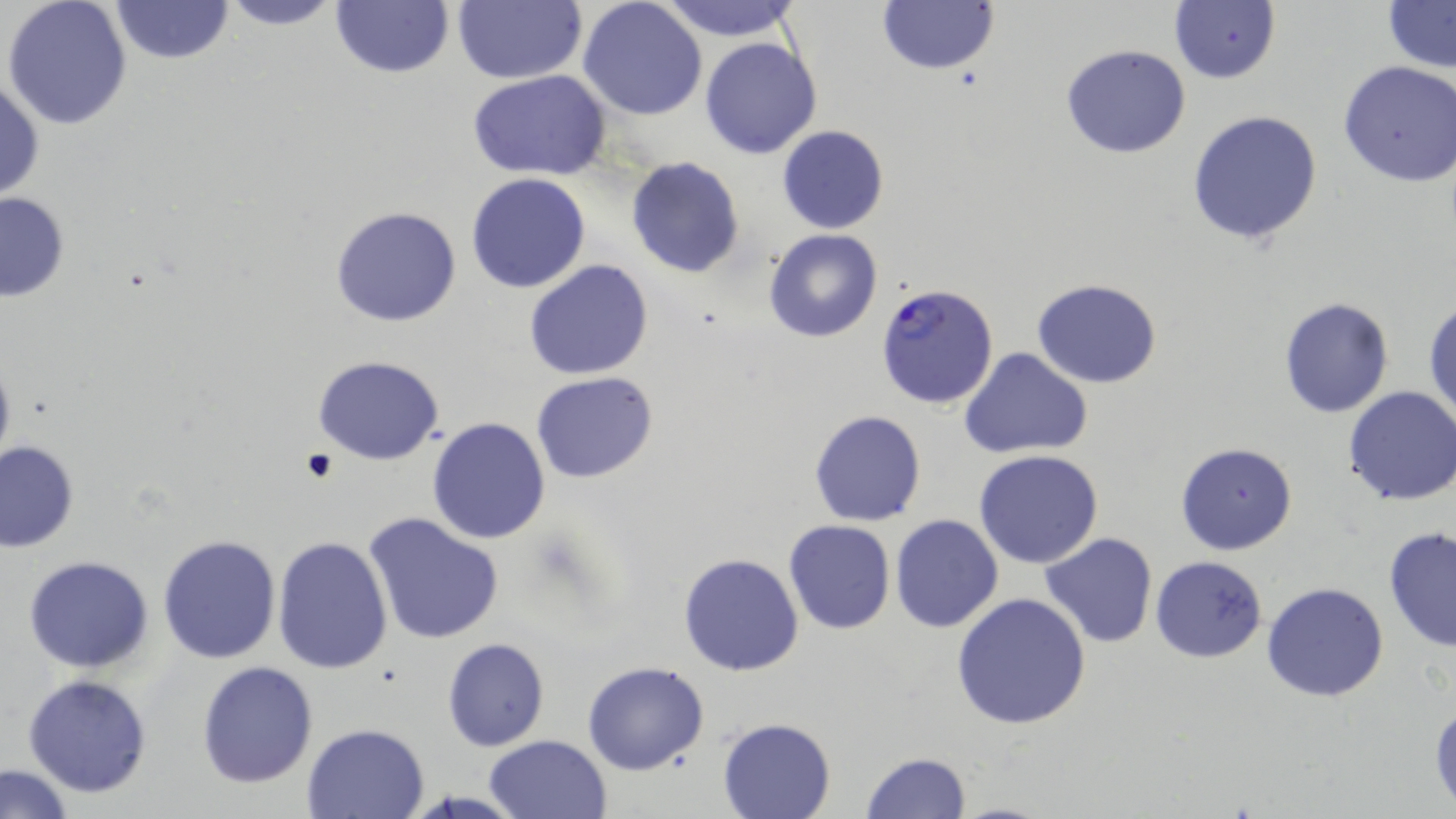
slide-level diagnosis = Plasmodium falciparum
stain = May-Grünwald-Giemsa
image size = 1456×819 pixels
preparation = thin blood film
magnification = 1000x
Plasmodium falciparum-infected red blood cell locations = approximate bounding boxes as (x1,y1)-(x2,y2) corner pairs in pixels: (876,282)-(1002,411)
field of view = one of a larger specimen
uninfected red blood cell locations = approximate bounding boxes as (x1,y1)-(x2,y2) corner pairs in pixels: (2,0)-(132,130), (216,0)-(347,30), (331,0)-(453,79), (453,0)-(586,85), (657,0)-(804,41), (110,1)-(235,65), (577,1)-(707,120), (878,1)-(1000,74), (1381,1)-(1456,72), (1169,2)-(1280,85), (700,36)-(822,158), (1060,44)-(1191,160), (1338,60)-(1456,187), (469,69)-(612,180), (0,75)-(44,203), (1187,110)-(1324,247), (776,125)-(890,234), (625,157)-(744,279), (466,172)-(593,293), (0,191)-(71,305), (331,205)-(463,328), (763,228)-(884,343), (524,259)-(654,381), (1032,278)-(1163,387), (1278,297)-(1395,418), (1425,298)-(1456,426), (960,345)-(1094,459), (0,352)-(16,475), (313,355)-(443,463), (531,372)-(659,484), (1342,386)-(1456,505), (808,409)-(927,527), (427,418)-(550,543), (1,441)-(78,553), (1175,441)-(1298,556), (975,450)-(1104,568), (364,512)-(506,646), (890,513)-(1004,633), (784,520)-(896,635), (1382,526)-(1456,653), (1040,531)-(1160,648), (157,533)-(282,665), (272,536)-(393,674), (678,552)-(805,676), (24,556)-(154,673), (1150,556)-(1268,662), (1262,581)-(1389,702), (950,591)-(1091,730), (442,638)-(550,751), (196,660)-(318,789), (582,661)-(709,775), (23,674)-(152,797), (1429,699)-(1456,810), (717,717)-(836,819), (302,722)-(431,818), (483,734)-(613,819), (860,752)-(973,819), (1,764)-(74,818)
modality = light microscopy